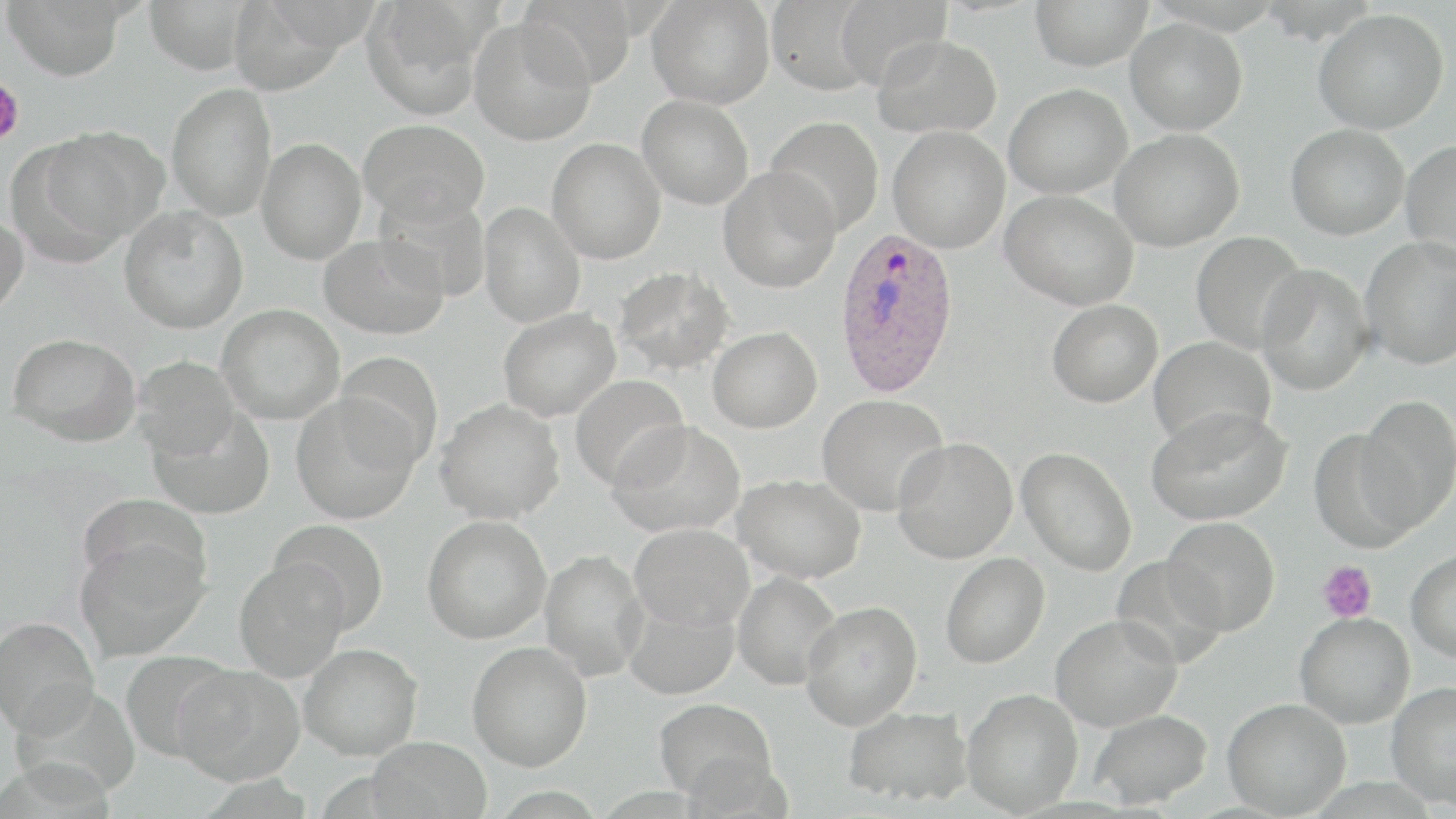 Approximate bounding boxes as [x1, y1, x2, y2] in pixels. Plasmodium ovale-infected red blood cell locations: [834, 230, 962, 399]. Platelet locations: [0, 69, 24, 152], [1317, 561, 1377, 623]. Uninfected red blood cell locations: [3, 0, 127, 82], [143, 0, 253, 75], [227, 0, 352, 96], [518, 0, 632, 92], [646, 0, 775, 109], [765, 0, 877, 95], [835, 0, 951, 92], [1030, 0, 1153, 71], [362, 1, 491, 119], [1314, 8, 1449, 135], [469, 17, 597, 145], [1125, 18, 1248, 136], [872, 34, 1003, 138], [166, 82, 277, 221], [1003, 84, 1132, 200], [637, 94, 754, 209], [765, 115, 884, 236], [359, 118, 490, 226], [1285, 124, 1409, 240], [887, 125, 1010, 253], [37, 126, 168, 246], [1110, 129, 1244, 251], [256, 138, 366, 264], [546, 138, 666, 264], [1401, 139, 1456, 263], [718, 167, 840, 293], [1001, 190, 1138, 310], [374, 191, 491, 301], [479, 202, 585, 328], [118, 206, 249, 333], [0, 210, 29, 318], [1191, 231, 1307, 355], [318, 234, 449, 340], [1360, 236, 1456, 370], [1255, 263, 1375, 396], [613, 265, 734, 375], [1047, 299, 1163, 407], [217, 304, 345, 424], [498, 308, 621, 421], [707, 326, 822, 433], [7, 332, 141, 445], [1148, 336, 1276, 448], [334, 351, 443, 470], [132, 354, 242, 458], [570, 374, 690, 490], [291, 394, 420, 525], [817, 394, 949, 516], [1355, 394, 1456, 533], [435, 399, 565, 523], [1146, 405, 1292, 526], [148, 407, 275, 519], [609, 421, 746, 537], [1310, 427, 1418, 551], [892, 437, 1018, 563], [1017, 448, 1137, 575], [733, 474, 866, 583], [422, 514, 552, 644], [1162, 516, 1280, 635], [271, 520, 390, 631], [629, 522, 754, 631], [74, 535, 209, 661], [1406, 547, 1456, 662], [539, 549, 648, 681], [941, 553, 1050, 668], [1111, 555, 1228, 668], [233, 557, 352, 681], [732, 571, 842, 690], [622, 594, 740, 700], [801, 600, 922, 729], [1295, 612, 1415, 728], [1050, 613, 1183, 731], [0, 616, 100, 737], [467, 641, 592, 770], [298, 643, 423, 760], [121, 651, 236, 764], [173, 666, 305, 784], [1386, 680, 1456, 807], [12, 685, 139, 801], [962, 688, 1083, 815], [653, 697, 778, 802], [1222, 698, 1351, 817], [843, 705, 973, 807], [1089, 708, 1212, 809], [366, 736, 493, 819]. Slide-level diagnosis: Plasmodium ovale. Light microscopy. One field of a larger specimen. Thin blood film. 1000x magnification. May-Grünwald-Giemsa stain. Image is 1456×819 pixels.